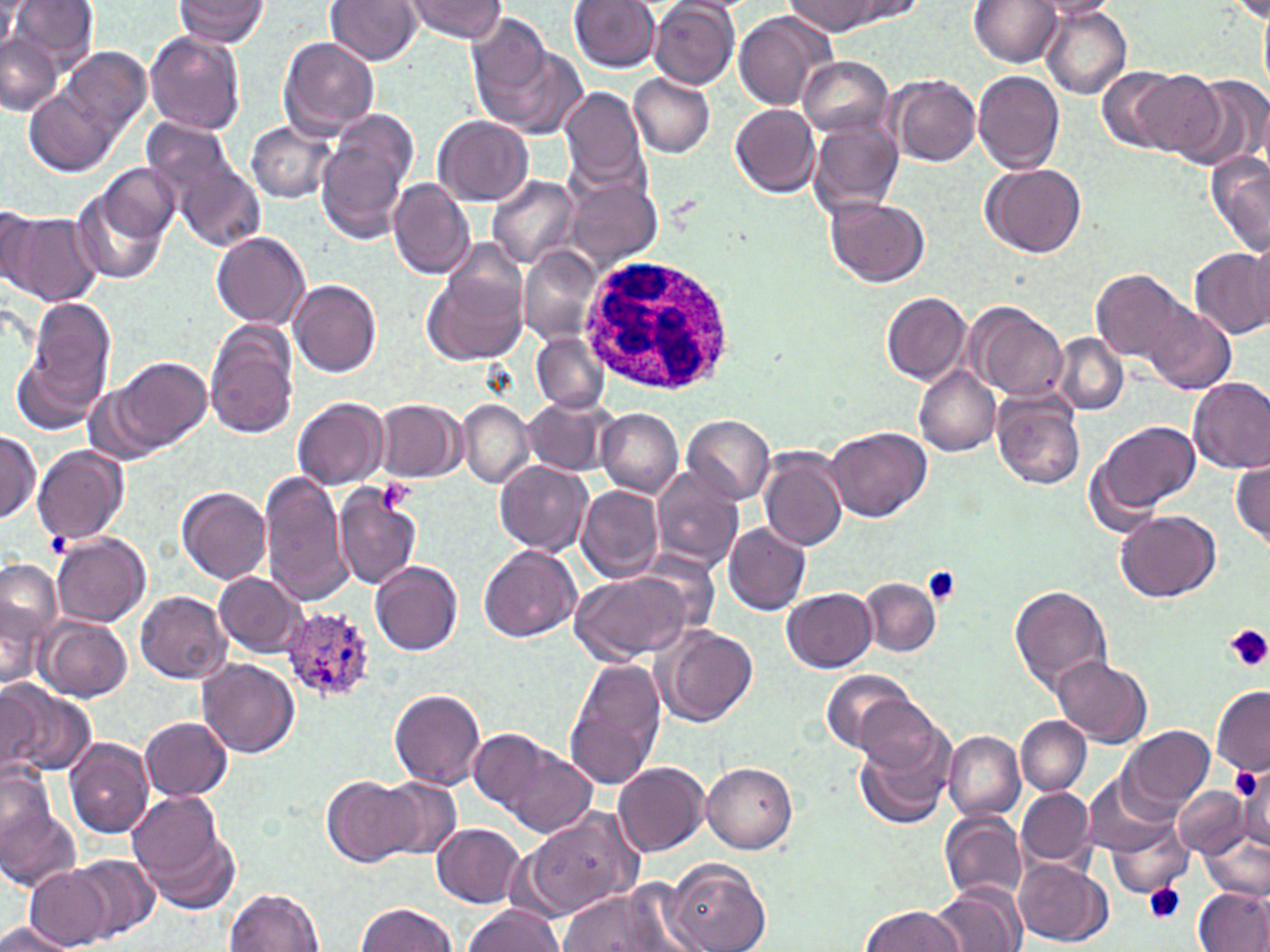

slide-level diagnosis = Plasmodium ovale
modality = optical microscopy
magnification = 1000x
platelet locations = approximate bounding boxes as [x1, y1, x2, y2] in pixels: [377, 478, 414, 513], [922, 566, 962, 606], [1224, 625, 1270, 672], [1229, 765, 1264, 804], [1143, 882, 1185, 923]
stain = May-Grünwald-Giemsa
preparation = thin blood smear
image size = 1270×952 pixels
white blood cell locations = approximate bounding boxes as [x1, y1, x2, y2] in pixels: [580, 252, 737, 398]
Plasmodium ovale-infected red blood cell locations = approximate bounding boxes as [x1, y1, x2, y2] in pixels: [281, 604, 378, 703]
uninfected red blood cell locations = approximate bounding boxes as [x1, y1, x2, y2] in pixels: [9, 0, 100, 74], [174, 0, 270, 45], [325, 0, 422, 66], [402, 0, 506, 43], [568, 0, 661, 72], [792, 0, 877, 35], [836, 0, 928, 25], [969, 0, 1064, 68], [1029, 0, 1121, 19], [0, 2, 27, 52], [650, 2, 739, 88], [1041, 8, 1133, 98], [734, 12, 833, 111], [467, 14, 558, 123], [145, 31, 246, 137], [1, 35, 61, 116], [278, 37, 379, 138], [61, 46, 150, 139], [486, 46, 589, 140], [797, 55, 896, 137], [1096, 65, 1185, 151], [972, 71, 1067, 173], [1123, 72, 1224, 157], [628, 73, 716, 158], [1180, 74, 1268, 169], [887, 76, 980, 167], [560, 85, 649, 191], [24, 87, 120, 177], [1250, 93, 1269, 179], [730, 104, 820, 196], [316, 117, 414, 247], [435, 117, 535, 206], [141, 118, 242, 216], [808, 119, 905, 217], [245, 122, 337, 203], [170, 151, 266, 251], [1207, 152, 1270, 259], [100, 162, 180, 243], [983, 162, 1086, 257], [487, 174, 579, 269], [564, 176, 660, 271], [70, 179, 173, 286], [388, 179, 475, 280], [827, 197, 931, 288], [0, 205, 41, 297], [6, 212, 103, 306], [211, 231, 310, 327], [1246, 235, 1270, 331], [1189, 247, 1270, 339], [520, 249, 602, 343], [425, 259, 526, 364], [1091, 269, 1191, 365], [292, 278, 384, 377], [882, 292, 970, 384], [24, 296, 116, 417], [967, 304, 1069, 402], [1147, 305, 1236, 395], [205, 319, 299, 440], [532, 333, 610, 413], [1053, 335, 1128, 414], [14, 352, 104, 435], [116, 356, 211, 451], [913, 364, 1002, 455], [1186, 375, 1270, 474], [83, 381, 166, 468], [993, 392, 1087, 490], [293, 396, 388, 490], [521, 397, 616, 476], [375, 398, 464, 483], [457, 401, 534, 489], [598, 409, 683, 496], [683, 415, 776, 505], [1093, 419, 1199, 519], [824, 425, 931, 521], [0, 431, 41, 525], [32, 444, 129, 545], [759, 447, 849, 553], [1232, 459, 1270, 546], [495, 461, 594, 556], [652, 467, 744, 573], [260, 471, 352, 606], [578, 485, 665, 582], [177, 486, 272, 584], [334, 489, 422, 590], [1114, 510, 1222, 603], [722, 520, 812, 615], [53, 533, 151, 626], [479, 545, 580, 642], [370, 560, 464, 655], [0, 566, 61, 690], [569, 567, 701, 664], [214, 572, 307, 657], [861, 578, 941, 657], [1009, 586, 1111, 693], [783, 587, 878, 672], [136, 591, 231, 686], [34, 615, 133, 701], [657, 626, 757, 727], [1053, 655, 1152, 747], [199, 658, 299, 757], [564, 658, 667, 791], [817, 668, 920, 754], [3, 683, 97, 778], [0, 685, 44, 778], [1212, 686, 1270, 775], [390, 688, 487, 790], [852, 695, 950, 783], [139, 716, 232, 801], [1016, 716, 1091, 796], [852, 724, 955, 830], [469, 726, 554, 812], [1121, 726, 1215, 815], [943, 729, 1026, 822], [64, 737, 153, 839], [499, 746, 597, 838], [72, 754, 183, 884], [613, 761, 709, 858], [703, 762, 797, 853], [0, 764, 58, 852], [1083, 770, 1182, 858], [1233, 774, 1270, 859], [322, 776, 417, 868], [376, 778, 461, 862], [1176, 785, 1250, 859], [1017, 786, 1096, 870], [126, 790, 237, 906], [0, 808, 80, 890], [523, 809, 642, 919], [940, 811, 1027, 902], [1103, 813, 1194, 900], [432, 823, 527, 908], [1201, 831, 1270, 901], [71, 855, 160, 941], [667, 858, 771, 952], [1015, 858, 1111, 947], [25, 866, 112, 950], [932, 882, 1026, 952], [1193, 886, 1270, 952], [558, 888, 681, 951], [225, 889, 325, 952], [357, 901, 456, 952], [462, 903, 562, 952], [862, 904, 962, 952], [1, 921, 75, 952]
field of view = single